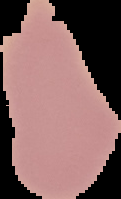
image type = cell region segmented out of the field of view; surrounding area masked to black
result = no Plasmodium parasites detected
image size = 121×199 pixels
preparation = thin blood smear